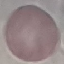
Summary:
  - Result: negative for malaria parasites
  - Image type: cell patch, automatically extracted from a larger field of view and resized to 64 × 64 pixels
  - Preparation: thin smear
  - Capture: smartphone camera at the microscope eyepiece
  - Stain: Giemsa